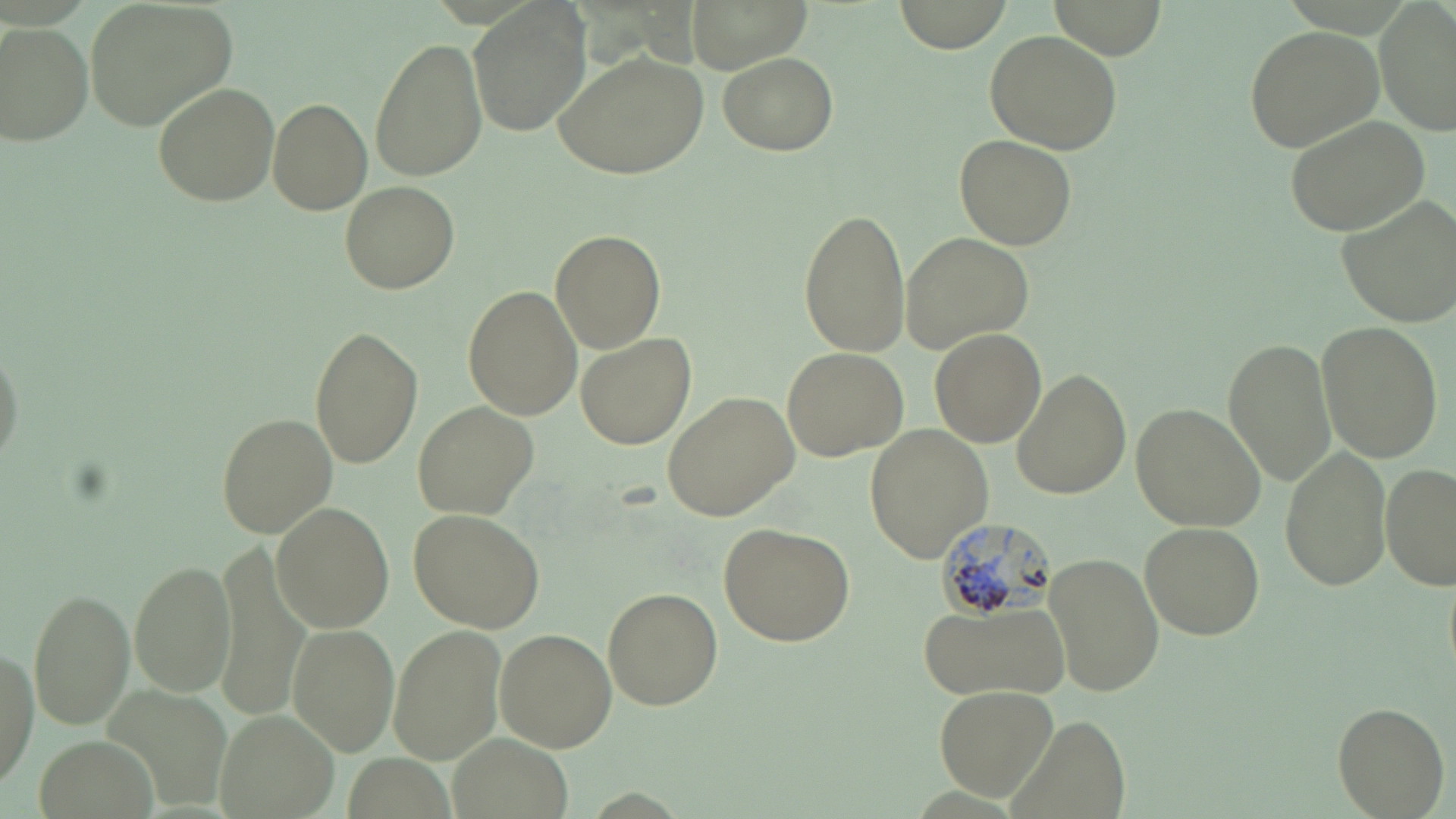
Approximate bounding boxes as (x1, y1, x2, y2) in pixels. Plasmodium malariae-infected red blood cell locations: (929, 518, 1059, 623). Uninfected red blood cell locations: (81, 0, 238, 131), (466, 0, 593, 137), (684, 0, 808, 73), (894, 0, 1015, 53), (1374, 1, 1455, 136), (2, 21, 95, 146), (1246, 23, 1385, 150), (984, 29, 1121, 153), (371, 37, 489, 183), (554, 49, 709, 179), (717, 52, 839, 156), (153, 81, 279, 208), (267, 97, 373, 217), (1281, 114, 1429, 237), (955, 135, 1075, 249), (340, 180, 460, 294), (1336, 197, 1456, 328), (798, 205, 909, 360), (549, 228, 667, 355), (902, 231, 1035, 353), (463, 284, 583, 420), (1314, 319, 1446, 465), (309, 324, 423, 470), (929, 327, 1047, 447), (574, 332, 696, 450), (1226, 335, 1340, 489), (780, 345, 908, 463), (1011, 367, 1132, 501), (661, 390, 800, 520), (413, 401, 538, 516), (1132, 403, 1267, 533), (218, 413, 338, 537), (864, 423, 993, 563), (1280, 446, 1392, 591), (1379, 462, 1455, 593), (270, 503, 394, 632), (409, 510, 545, 631), (720, 522, 856, 647), (1140, 523, 1265, 641), (211, 534, 317, 714), (1042, 551, 1165, 696), (128, 559, 237, 701), (27, 587, 135, 731), (603, 587, 723, 709), (921, 602, 1072, 701), (287, 622, 400, 756), (387, 625, 507, 767), (494, 628, 617, 752), (1, 637, 38, 790), (933, 683, 1063, 801), (1331, 701, 1448, 816), (213, 707, 342, 818), (1005, 713, 1132, 819), (36, 731, 157, 819), (441, 733, 576, 819). Slide-level diagnosis: Plasmodium malariae. Single field of view. Thin blood smear. Optical microscopy. 1000x magnification. Image is 1456×819 pixels. May-Grünwald-Giemsa-stained preparation.